Assess this cell for malaria.
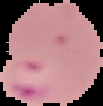

Parasitized.

preparation = thin blood film
image size = 103×106 pixels
image type = segmented cell region with the area outside set to black